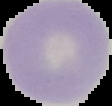

Segmented cell region on a black background. Malaria status: uninfected. From a thin blood film. Image is 112×106 pixels.